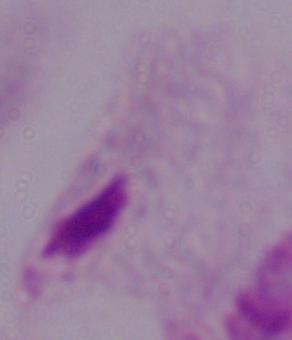
Summary:
  - Identification: trichomonad
  - Modality: photomicrograph
  - Magnification: 1000x